Report the malaria status.
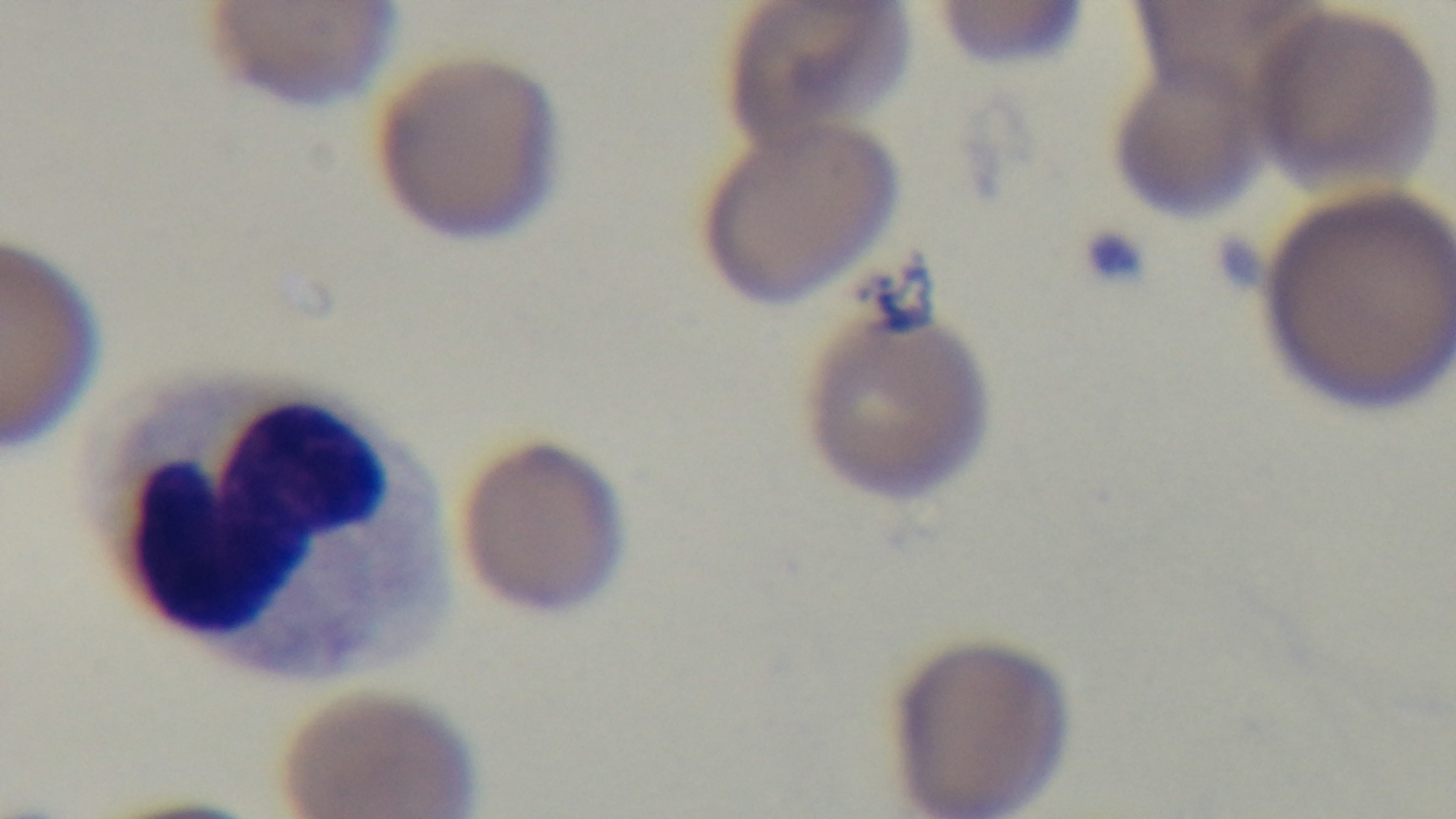

It is infected.

Summary:
  - Objective: 100x oil immersion
  - Field of view: one from the slide
  - Preparation: thin
  - Stain: Giemsa
  - Modality: light microscopy
  - Capture: mounted 4K digital camera